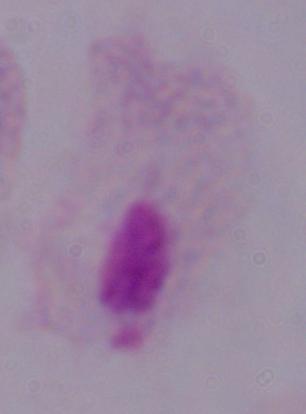

modality = micrograph
identification = trichomonad
magnification = 1000x